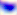
Summary:
  - Modality: micrograph
  - Identification: Toxoplasma gondii
  - Magnification: 400x